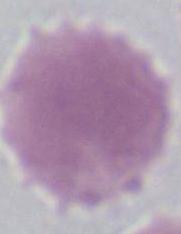
{
  "identification": "erythrocyte",
  "magnification": "1000x",
  "modality": "photomicrograph"
}